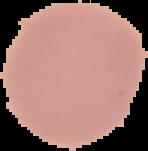

malaria status = uninfected
image type = segmented cell region on a black background
image size = 148×151 pixels
preparation = thin blood film